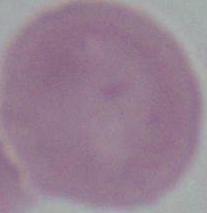
Captured at 1000x magnification. An erythrocyte is seen. Photomicrograph.